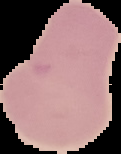

preparation = thin blood smear
malaria status = uninfected
image type = segmented cell region on a black background
image size = 121×154 pixels